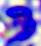
modality = micrograph
magnification = 400x
identification = leukocyte